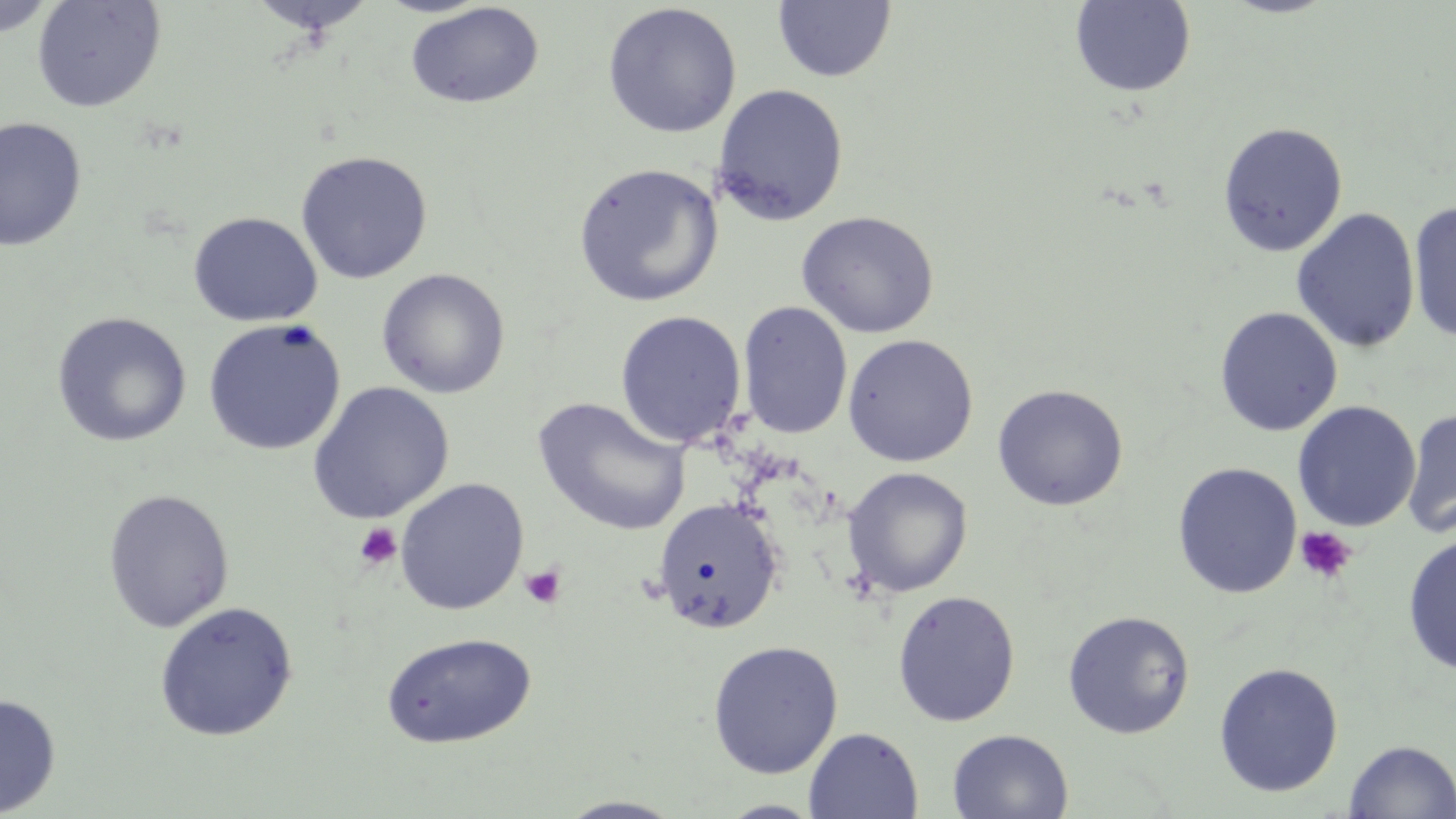
Approximate bounding boxes as named x1/y1/x2/y2 corners in pixels. Platelet locations: (x1=354, y1=522, x2=402, y2=570), (x1=1294, y1=526, x2=1357, y2=584), (x1=520, y1=564, x2=566, y2=608). Uninfected red blood cell locations: (x1=0, y1=0, x2=60, y2=38), (x1=31, y1=0, x2=166, y2=113), (x1=245, y1=0, x2=379, y2=37), (x1=1070, y1=0, x2=1197, y2=98), (x1=772, y1=1, x2=896, y2=84), (x1=404, y1=2, x2=545, y2=110), (x1=602, y1=3, x2=742, y2=138), (x1=712, y1=83, x2=849, y2=226), (x1=0, y1=116, x2=87, y2=253), (x1=1218, y1=121, x2=1348, y2=257), (x1=294, y1=150, x2=433, y2=284), (x1=573, y1=162, x2=724, y2=307), (x1=1408, y1=202, x2=1456, y2=343), (x1=1291, y1=208, x2=1420, y2=353), (x1=796, y1=210, x2=939, y2=338), (x1=188, y1=212, x2=322, y2=327), (x1=376, y1=268, x2=510, y2=398), (x1=737, y1=301, x2=853, y2=439), (x1=1214, y1=306, x2=1342, y2=436), (x1=614, y1=310, x2=747, y2=448), (x1=51, y1=312, x2=193, y2=447), (x1=202, y1=318, x2=347, y2=456), (x1=842, y1=333, x2=979, y2=467), (x1=307, y1=382, x2=455, y2=525), (x1=991, y1=384, x2=1129, y2=511), (x1=532, y1=397, x2=692, y2=537), (x1=1293, y1=400, x2=1421, y2=532), (x1=1402, y1=406, x2=1456, y2=539), (x1=1172, y1=462, x2=1303, y2=599), (x1=842, y1=467, x2=973, y2=597), (x1=394, y1=479, x2=529, y2=615), (x1=102, y1=488, x2=235, y2=633), (x1=653, y1=497, x2=784, y2=634), (x1=1402, y1=533, x2=1456, y2=676), (x1=892, y1=589, x2=1021, y2=727), (x1=154, y1=602, x2=299, y2=742), (x1=1062, y1=609, x2=1195, y2=739), (x1=380, y1=632, x2=537, y2=748), (x1=707, y1=640, x2=844, y2=779), (x1=1213, y1=662, x2=1344, y2=798), (x1=0, y1=693, x2=61, y2=817), (x1=804, y1=727, x2=923, y2=818), (x1=947, y1=728, x2=1073, y2=818), (x1=1344, y1=740, x2=1456, y2=818), (x1=555, y1=797, x2=689, y2=818), (x1=717, y1=799, x2=826, y2=818). Slide-level diagnosis: no evidence of blood parasites. May-Grünwald-Giemsa stain. Image is 1456×819 pixels. One field of a larger specimen. 1000x magnification. Light microscopy. Thin blood film.